Assess this cell for malaria.
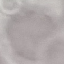
It is uninfected.

Acquired by smartphone through the microscope eyepiece. Thin blood smear. Giemsa-stained preparation. Cell patch, automatically extracted from a larger field of view and resized to 64 × 64 pixels.